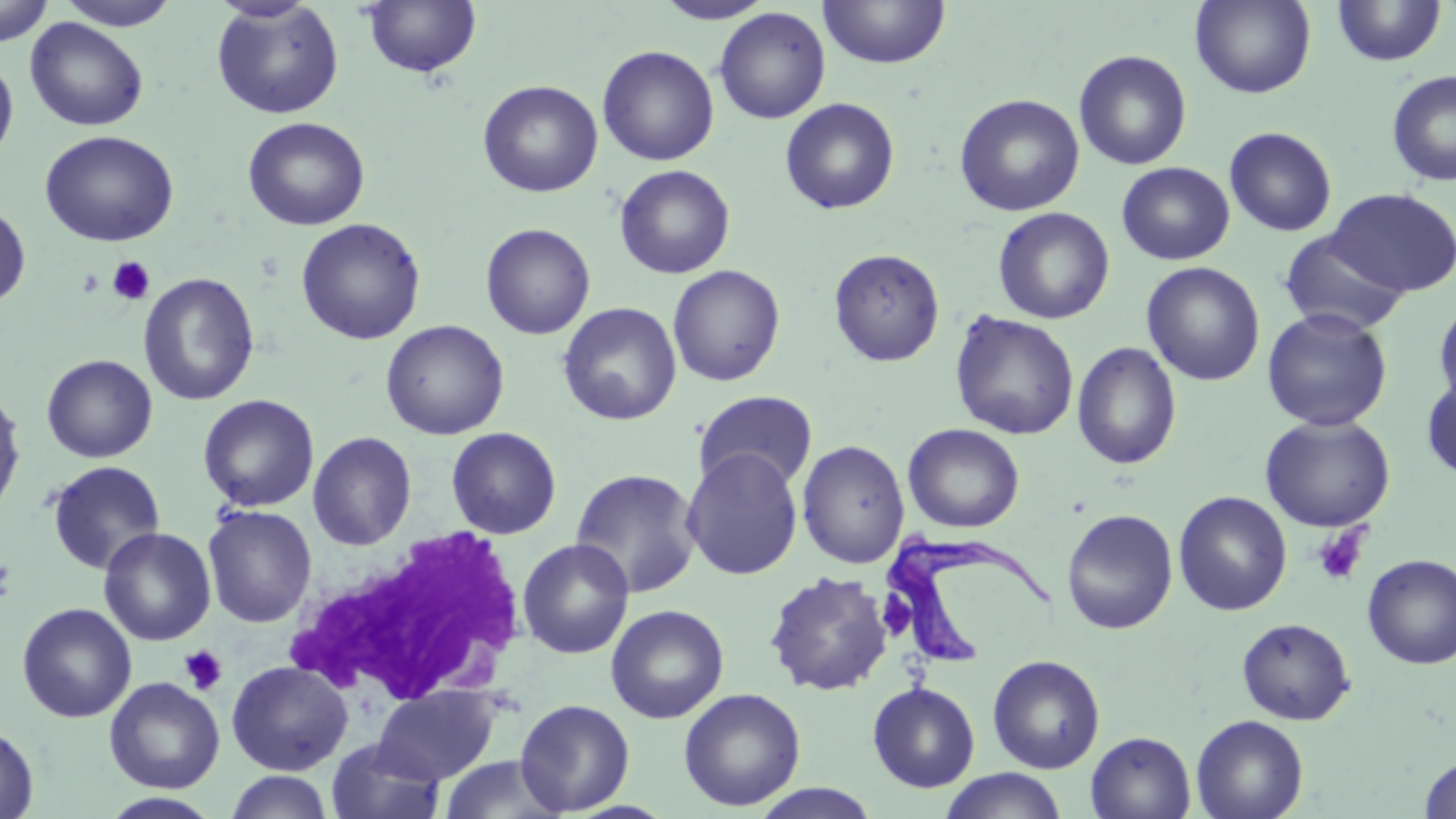
Approximate bounding boxes as (x1, y1, x2, y2) in pixels. Platelet locations: (106, 257, 156, 306), (1311, 525, 1368, 587), (0, 557, 16, 603), (179, 645, 227, 697). Uninfected red blood cell locations: (0, 0, 54, 47), (58, 0, 177, 29), (817, 0, 951, 69), (1190, 0, 1316, 99), (210, 1, 344, 119), (654, 1, 775, 24), (1331, 1, 1447, 67), (362, 2, 482, 78), (713, 7, 831, 124), (25, 17, 149, 132), (597, 45, 720, 166), (1073, 49, 1193, 170), (0, 54, 19, 165), (1386, 69, 1456, 187), (477, 80, 603, 197), (953, 93, 1085, 217), (779, 97, 900, 215), (242, 116, 370, 231), (1224, 126, 1337, 237), (39, 130, 179, 247), (1117, 162, 1234, 265), (614, 164, 736, 279), (1327, 187, 1455, 296), (0, 203, 32, 308), (992, 206, 1115, 324), (295, 217, 427, 345), (480, 223, 596, 340), (1278, 232, 1411, 336), (828, 248, 945, 366), (1141, 261, 1266, 386), (667, 264, 786, 386), (138, 272, 260, 407), (1433, 300, 1456, 413), (558, 302, 682, 426), (1261, 307, 1393, 432), (949, 311, 1080, 440), (380, 319, 510, 440), (1071, 342, 1182, 470), (42, 354, 158, 463), (1421, 371, 1456, 484), (0, 386, 26, 521), (692, 390, 818, 494), (198, 394, 320, 512), (1259, 414, 1396, 532), (903, 422, 1025, 533), (446, 426, 562, 539), (308, 431, 417, 550), (797, 439, 911, 568), (681, 448, 803, 581), (46, 461, 166, 574), (570, 467, 702, 599), (1172, 490, 1292, 616), (202, 505, 318, 627), (1061, 508, 1178, 634), (98, 527, 216, 645), (517, 538, 635, 659), (1361, 553, 1456, 669), (763, 570, 894, 696), (16, 602, 137, 723), (605, 604, 730, 724), (1236, 617, 1355, 725), (987, 655, 1106, 774), (226, 660, 353, 775), (104, 677, 225, 793), (868, 682, 980, 793), (372, 686, 502, 785), (678, 688, 806, 811), (515, 698, 635, 815), (1190, 714, 1308, 819), (0, 724, 39, 819), (1085, 732, 1197, 818), (325, 739, 447, 819), (438, 755, 569, 818), (1419, 755, 1456, 818), (938, 769, 1069, 819), (223, 770, 335, 819), (748, 784, 883, 819), (99, 792, 223, 818). White blood cell locations: (289, 526, 531, 709). Trypanosoma brucei locations: (880, 536, 1057, 670). Slide-level diagnosis: Trypanosoma brucei. Thin blood smear. 1000x magnification. Image is 1456×819 pixels. May-Grünwald-Giemsa stain. Single field of view. Light microscopy.